State which parasite is depicted.
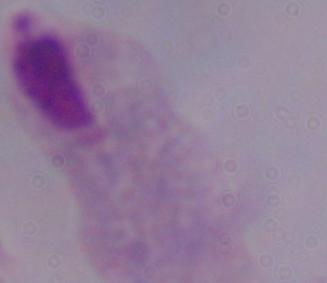

A trichomonad.

1000x magnification. Photomicrograph.